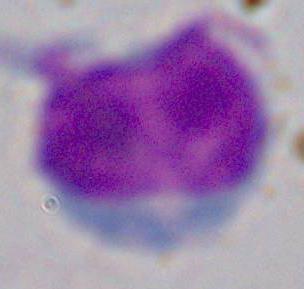
modality: photomicrograph
magnification: 1000x
identification: white blood cell